Report the malaria status.
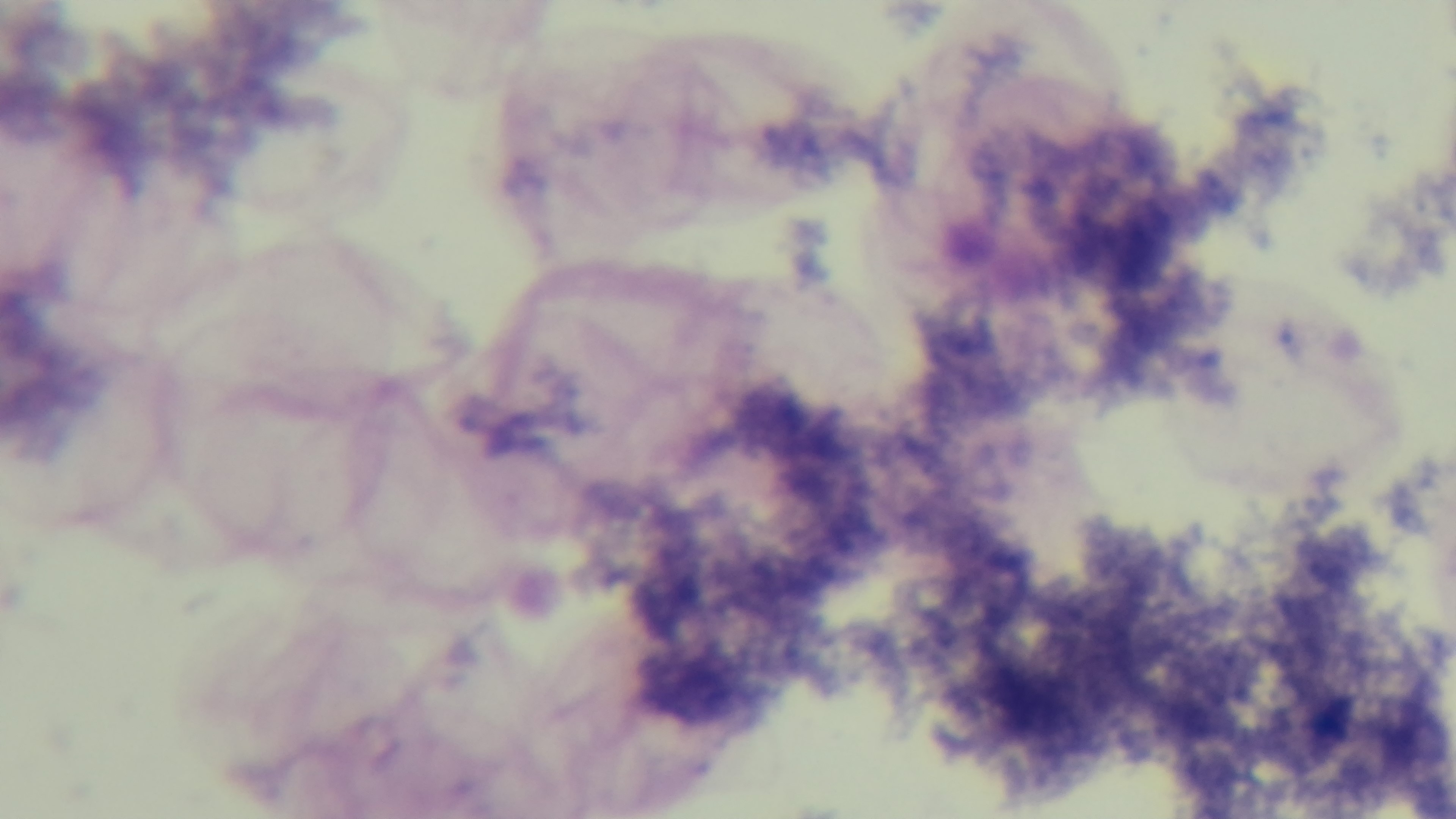
Negative.

Summary:
  - Capture: mounted 4K digital camera
  - Objective: 100x oil immersion
  - Preparation: thick blood film
  - Modality: light microscopy
  - Stain: Giemsa
  - Field of view: one from the slide